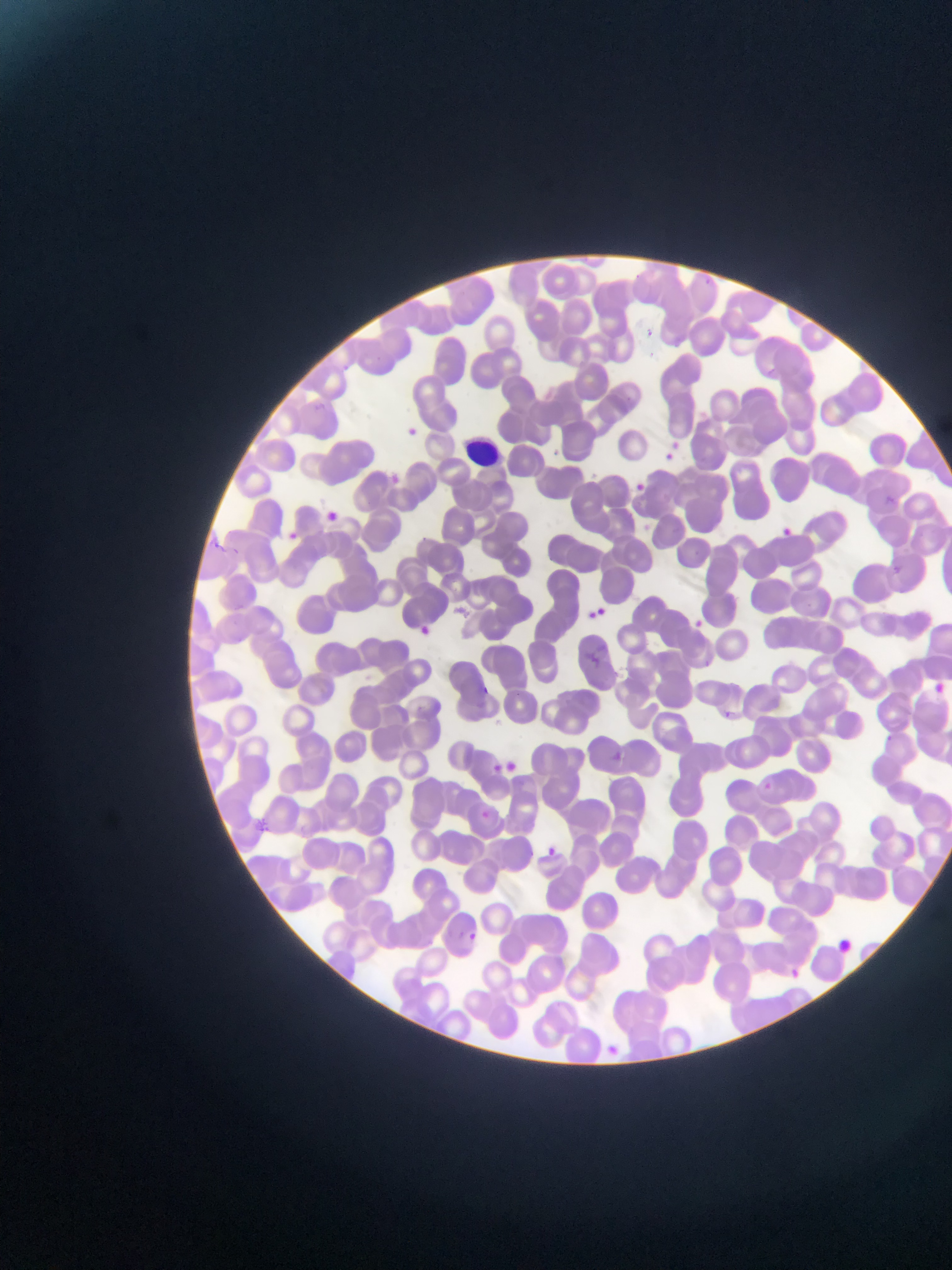

Approximate bounding boxes as (left, top, right, bottom) in pixels. Malaria parasite locations: (702, 274, 716, 288), (642, 322, 652, 340), (404, 422, 419, 439), (669, 437, 681, 450), (550, 447, 561, 457), (662, 452, 678, 469), (392, 469, 406, 484), (634, 483, 648, 501), (326, 507, 340, 521), (784, 524, 798, 540), (288, 528, 302, 543), (891, 563, 901, 573), (590, 607, 608, 623), (693, 615, 700, 627), (417, 622, 430, 635), (701, 654, 710, 668), (934, 678, 947, 700), (483, 684, 494, 695), (722, 710, 735, 723), (883, 732, 894, 748), (607, 748, 632, 765), (495, 761, 510, 776), (508, 761, 527, 778), (764, 778, 770, 788), (480, 809, 490, 817), (547, 845, 555, 854), (468, 924, 479, 942), (790, 965, 800, 979), (604, 1041, 621, 1058). Leukocyte locations: (464, 429, 505, 471). One field of view. Image is 952×1270 pixels. Collected in Ghana. Thin blood smear. Mobile-phone photograph taken through the microscope.